Name the parasite shown.
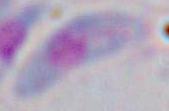

Toxoplasma gondii.

Summary:
  - Magnification: 1000x
  - Modality: photomicrograph